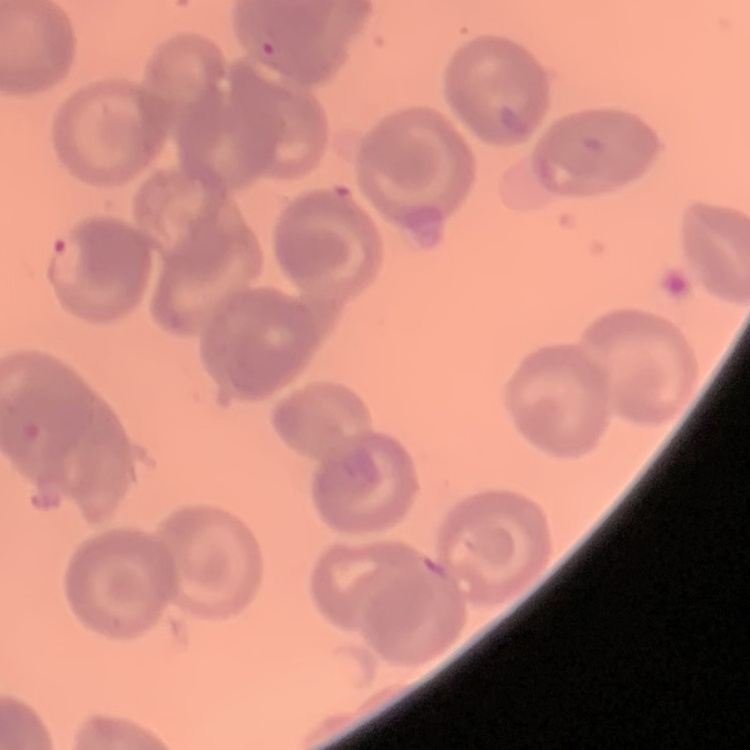
erythrocyte morphology = no rouleaux formation
preparation = thin peripheral smear
image type = one tile cut from a larger photomicrograph
stain = Field's or Giemsa